State the preparation type.
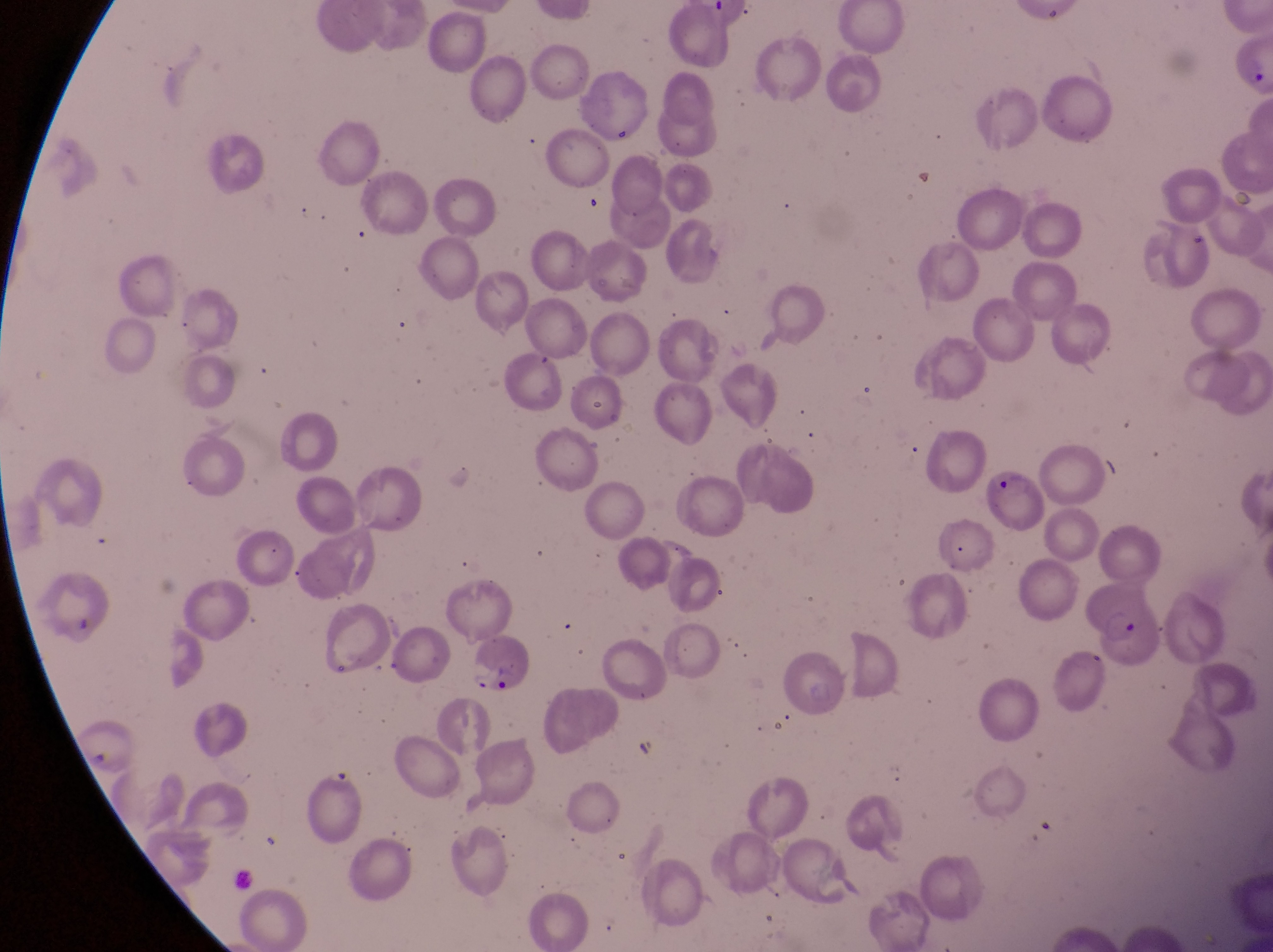

Thin blood film.

Approximate bounding boxes as (left, top, right, bottom) in pixels.
Summary:
  - Parasitised red blood cell locations: (984, 464, 1051, 532), (1081, 577, 1166, 670), (469, 634, 536, 697), (299, 757, 368, 849)
  - Magnification: 1000x
  - Country: Uganda
  - Capture: smartphone photograph through the eyepiece of an Olympus CX-23 microscope
  - Field of view: single
  - Image size: 1273×952 pixels